State which parasite is depicted.
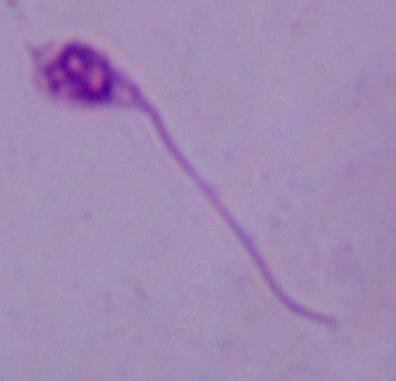
This is Leishmania.

Summary:
  - Magnification: 1000x
  - Modality: photomicrograph